Give the position of every malaria parasite.
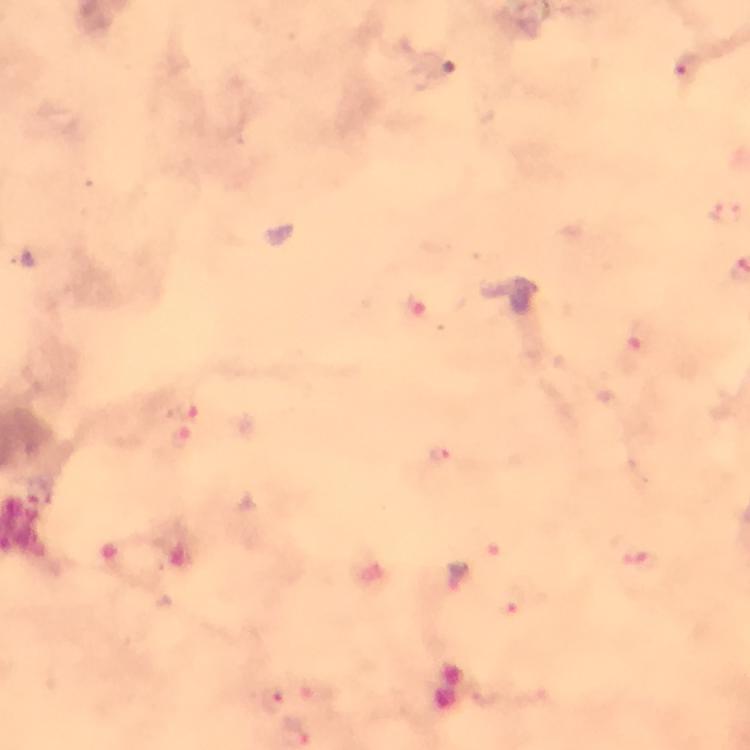

Approximate centers as (x, y) in pixels.
Malaria parasites: (688, 69), (180, 412), (180, 438), (441, 456), (640, 562), (514, 604), (272, 701).

Giemsa-stained preparation. Immersion oil applied. From a diagnostic examination for malaria. Thick blood film. At 100x magnification. Cropped region of a single field of view. Photographed through the microscope with a smartphone camera. Image is 750×750 pixels.